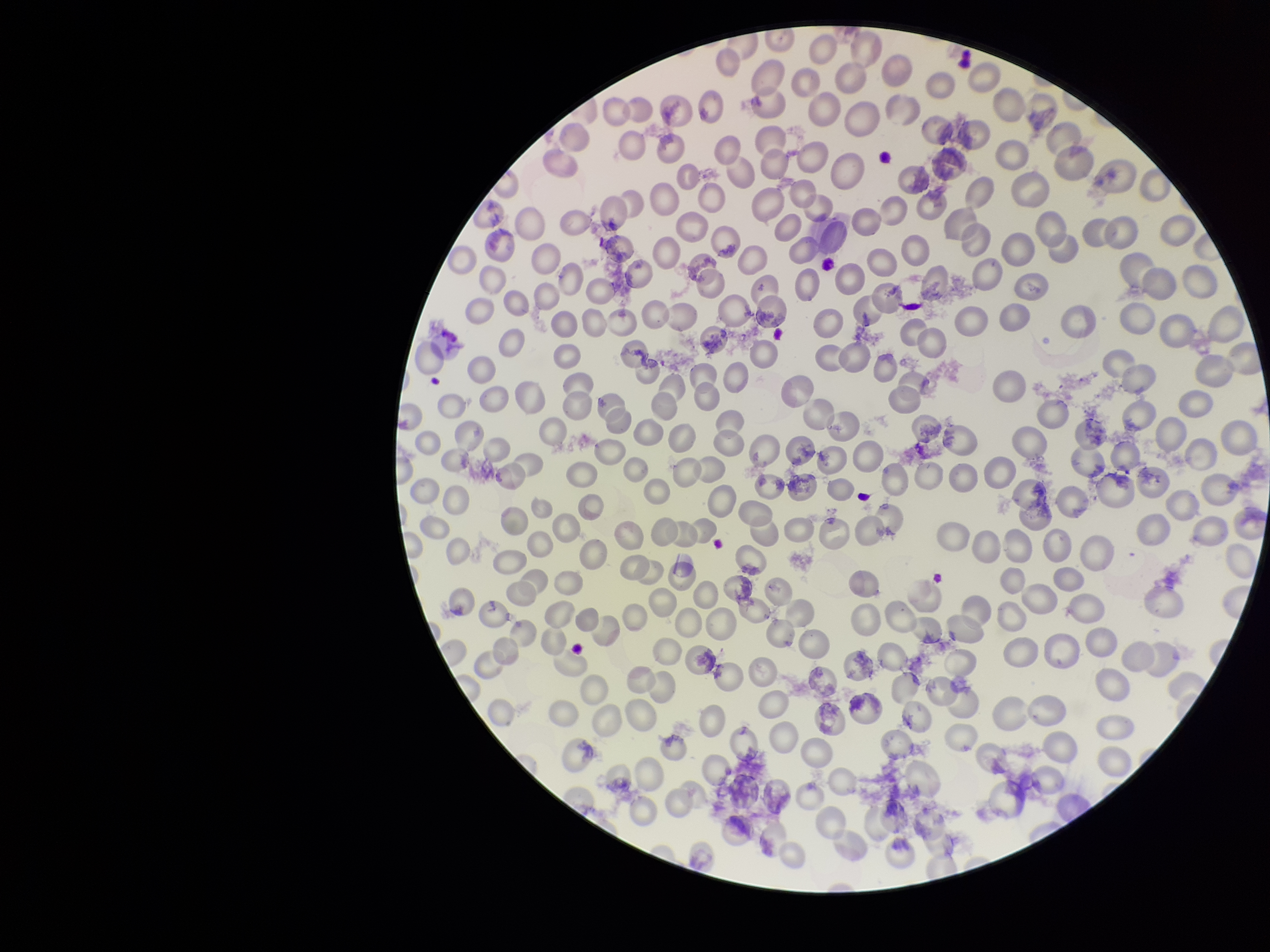
field of view = one from this slide
patient malaria status = negative
stain = Giemsa
parasitized red blood cell count = 0
image size = 1270×952 pixels
preparation = thin blood smear
red blood cell count = 260
capture = smartphone photograph through the microscope eyepiece
parasitized red blood cells = none detected